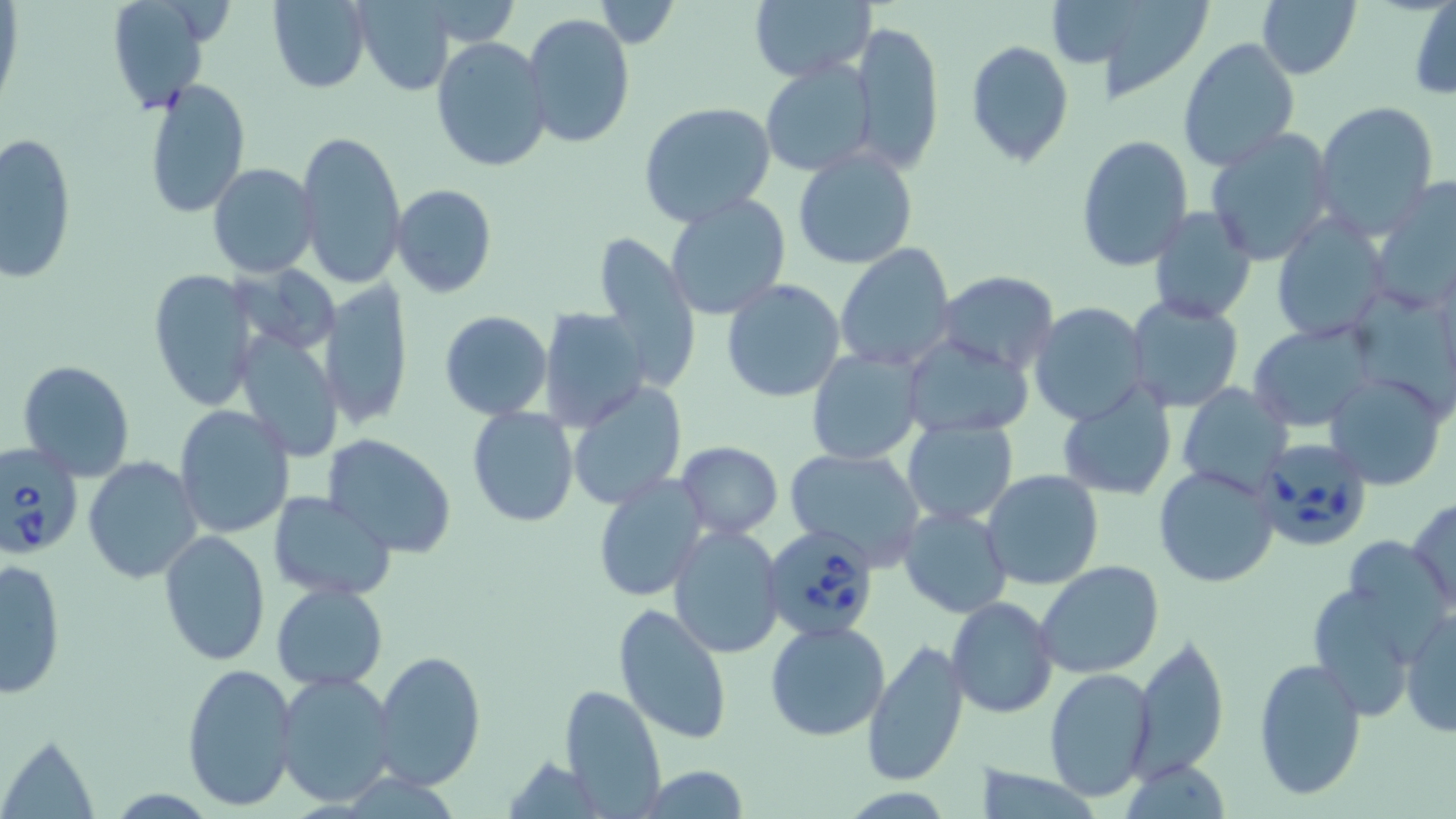
{
  "slide_level_diagnosis": "Babesia divergens",
  "modality": "optical microscopy",
  "babesia_divergens_infected_red_blood_cell_locations": "approximate bounding boxes as named x1/y1/x2/y2 corners in pixels: (x1=1252, y1=437, x2=1374, y2=555), (x1=0, y1=443, x2=83, y2=560), (x1=762, y1=524, x2=881, y2=645)",
  "preparation": "thin blood smear",
  "magnification": "1000x",
  "image_size": "1456×819 pixels",
  "field_of_view": "single",
  "stain": "May-Grünwald-Giemsa",
  "uninfected_red_blood_cell_locations": "approximate bounding boxes as named x1/y1/x2/y2 corners in pixels: (x1=103, y1=0, x2=217, y2=113), (x1=267, y1=0, x2=374, y2=93), (x1=1080, y1=0, x2=1219, y2=103), (x1=1256, y1=0, x2=1361, y2=80), (x1=356, y1=1, x2=454, y2=95), (x1=592, y1=1, x2=679, y2=47), (x1=748, y1=1, x2=872, y2=82), (x1=1409, y1=3, x2=1456, y2=102), (x1=523, y1=13, x2=635, y2=150), (x1=849, y1=22, x2=944, y2=172), (x1=431, y1=37, x2=554, y2=174), (x1=1177, y1=38, x2=1301, y2=176), (x1=965, y1=39, x2=1075, y2=168), (x1=759, y1=59, x2=878, y2=177), (x1=142, y1=77, x2=251, y2=219), (x1=1313, y1=102, x2=1438, y2=232), (x1=640, y1=103, x2=777, y2=229), (x1=1205, y1=129, x2=1335, y2=265), (x1=295, y1=130, x2=406, y2=290), (x1=3, y1=132, x2=77, y2=282), (x1=1076, y1=135, x2=1194, y2=270), (x1=792, y1=146, x2=918, y2=268), (x1=208, y1=163, x2=318, y2=277), (x1=1370, y1=178, x2=1456, y2=316), (x1=392, y1=183, x2=498, y2=298), (x1=664, y1=193, x2=792, y2=321), (x1=1148, y1=206, x2=1258, y2=323), (x1=1271, y1=216, x2=1389, y2=344), (x1=589, y1=233, x2=700, y2=390), (x1=835, y1=243, x2=958, y2=372), (x1=148, y1=269, x2=262, y2=412), (x1=936, y1=272, x2=1059, y2=374), (x1=721, y1=278, x2=846, y2=403), (x1=321, y1=280, x2=413, y2=430), (x1=1124, y1=295, x2=1246, y2=414), (x1=1029, y1=303, x2=1151, y2=427), (x1=538, y1=306, x2=651, y2=433), (x1=439, y1=310, x2=553, y2=420), (x1=1245, y1=322, x2=1377, y2=432), (x1=234, y1=332, x2=345, y2=461), (x1=902, y1=333, x2=1035, y2=438), (x1=806, y1=347, x2=925, y2=465), (x1=18, y1=360, x2=135, y2=482), (x1=1325, y1=371, x2=1451, y2=491), (x1=567, y1=381, x2=687, y2=509), (x1=1173, y1=382, x2=1291, y2=496), (x1=1056, y1=388, x2=1177, y2=501), (x1=174, y1=403, x2=295, y2=540), (x1=465, y1=406, x2=580, y2=528), (x1=900, y1=417, x2=1019, y2=527), (x1=321, y1=434, x2=457, y2=558), (x1=677, y1=441, x2=783, y2=538), (x1=783, y1=448, x2=926, y2=569), (x1=81, y1=455, x2=203, y2=586), (x1=1154, y1=465, x2=1280, y2=588), (x1=982, y1=469, x2=1103, y2=591), (x1=592, y1=473, x2=708, y2=605), (x1=268, y1=491, x2=399, y2=601), (x1=1407, y1=497, x2=1456, y2=617), (x1=898, y1=506, x2=1013, y2=618), (x1=1367, y1=516, x2=1456, y2=636), (x1=666, y1=523, x2=785, y2=659), (x1=157, y1=529, x2=270, y2=667), (x1=1, y1=557, x2=68, y2=698), (x1=1035, y1=559, x2=1166, y2=678), (x1=1304, y1=582, x2=1427, y2=720), (x1=271, y1=583, x2=388, y2=692), (x1=946, y1=597, x2=1059, y2=718), (x1=612, y1=602, x2=734, y2=744), (x1=1401, y1=609, x2=1456, y2=737), (x1=765, y1=620, x2=891, y2=740), (x1=1131, y1=635, x2=1231, y2=780), (x1=861, y1=638, x2=971, y2=787), (x1=374, y1=651, x2=485, y2=791), (x1=1252, y1=656, x2=1367, y2=802), (x1=181, y1=662, x2=299, y2=812), (x1=1044, y1=667, x2=1157, y2=801), (x1=275, y1=671, x2=399, y2=807), (x1=558, y1=684, x2=667, y2=816), (x1=2, y1=732, x2=102, y2=817), (x1=1120, y1=759, x2=1234, y2=816), (x1=636, y1=765, x2=751, y2=819)"
}